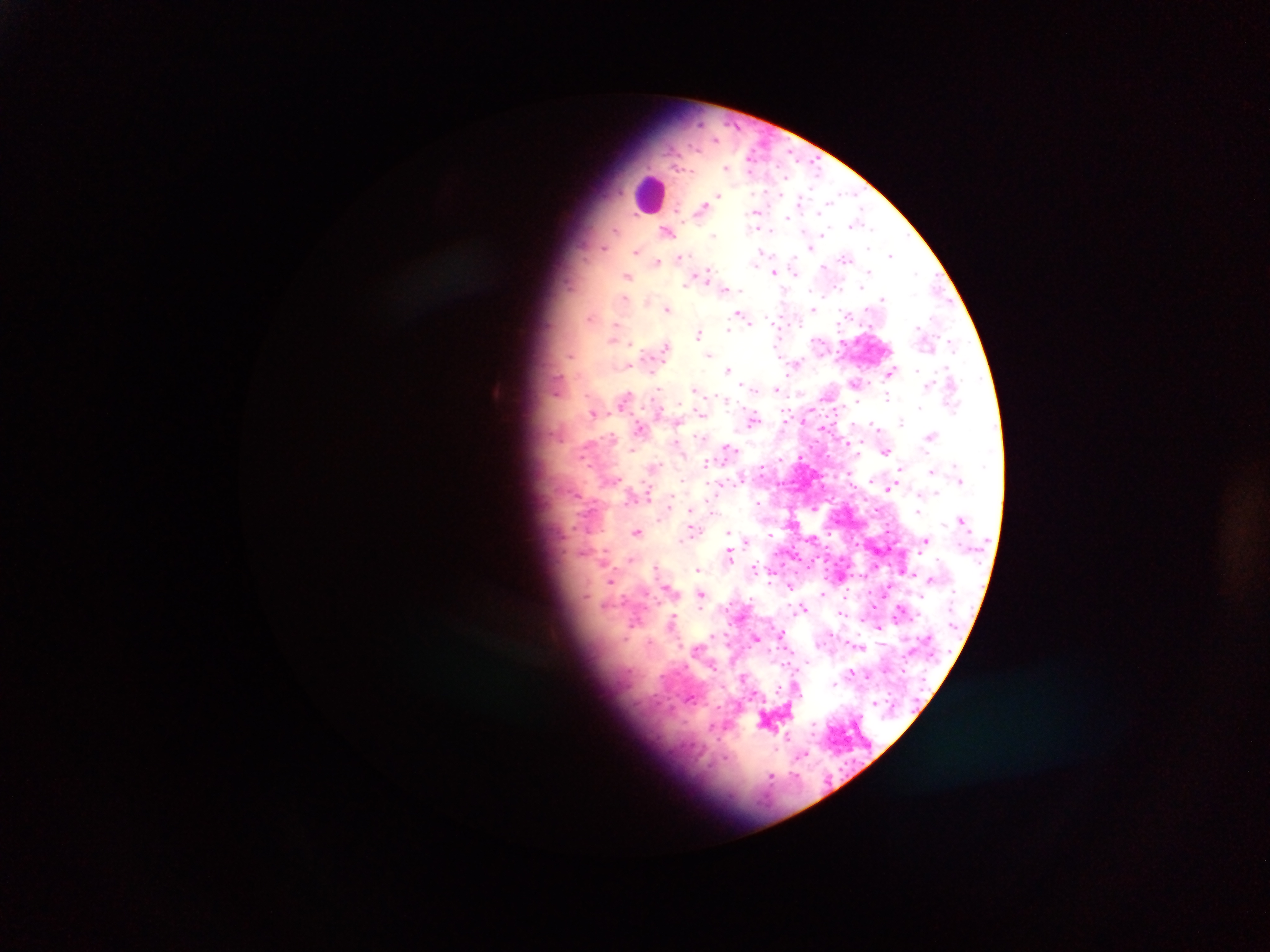
Approximate centers as [x, y] in pixels. Leukocyte locations: [645, 196]. Malaria parasite locations: [727, 168], [817, 168], [718, 194], [828, 202], [852, 225], [755, 228], [668, 231], [823, 231], [870, 232], [715, 234], [604, 246], [814, 249], [638, 250], [890, 255], [847, 258], [658, 260], [793, 272], [773, 273], [869, 273], [916, 273], [626, 276], [883, 297], [625, 300], [646, 301], [666, 308], [814, 308], [739, 314], [591, 317], [743, 317], [771, 318], [728, 330], [699, 332], [613, 338], [630, 344], [952, 345], [710, 353], [569, 355], [797, 365], [626, 366], [728, 370], [890, 372], [927, 385], [775, 388], [694, 392], [889, 396], [723, 397], [626, 398], [856, 402], [920, 406], [593, 412], [752, 419], [901, 421], [873, 428], [640, 429], [932, 434], [847, 443], [727, 446], [885, 450], [736, 452], [860, 452], [802, 459], [706, 463], [932, 470], [681, 479], [743, 484], [886, 488], [892, 488], [676, 497], [756, 505], [811, 508], [689, 510], [920, 513], [638, 531], [729, 532], [831, 533], [770, 537], [680, 541], [923, 542], [605, 553], [730, 555], [629, 559], [813, 564], [700, 567], [655, 568], [808, 568], [770, 574], [796, 574], [909, 574], [610, 580], [791, 588], [671, 590], [702, 595], [623, 599], [805, 608], [901, 609], [671, 622], [878, 628], [780, 633], [756, 638], [858, 647], [833, 685], [802, 756], [772, 774]. Mobile-phone photograph taken through the microscope. One field of view. Thick blood film. Sample from Ghana. Image is 1270×952 pixels.